Identify the parasite.
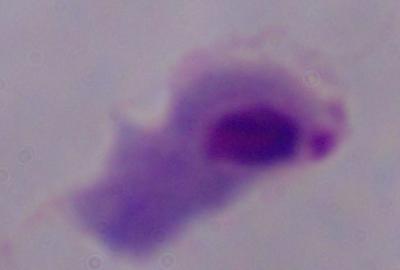
A trichomonad.

Summary:
  - Magnification: 1000x
  - Modality: micrograph